Locate every uninfected red blood cell.
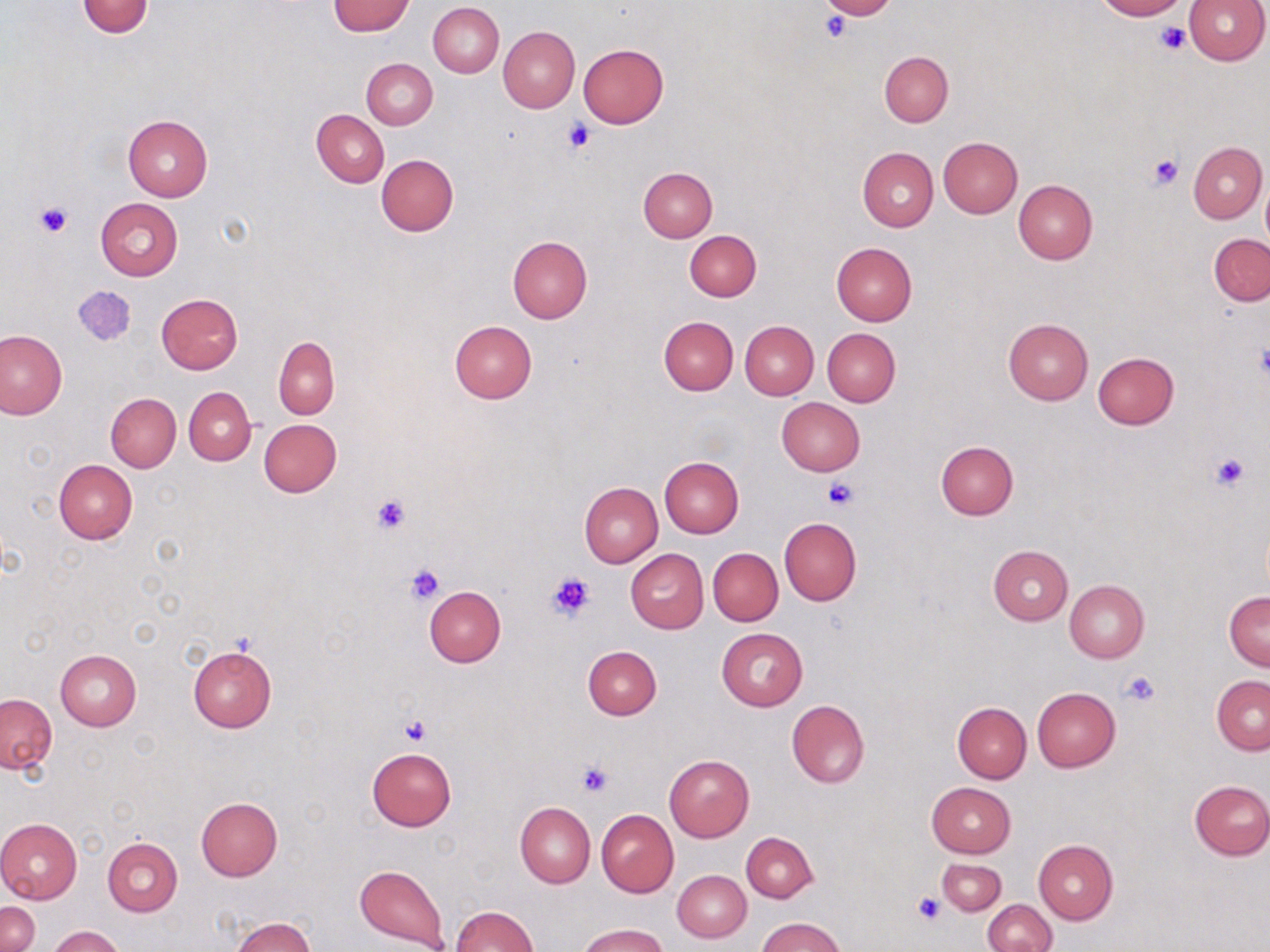
Approximate bounding boxes as named x1/y1/x2/y2 corners in pixels.
Uninfected red blood cells: (x1=819, y1=0, x2=898, y2=20), (x1=1093, y1=0, x2=1188, y2=20), (x1=1182, y1=0, x2=1269, y2=64), (x1=75, y1=1, x2=154, y2=38), (x1=327, y1=1, x2=414, y2=35), (x1=428, y1=3, x2=504, y2=78), (x1=499, y1=26, x2=579, y2=113), (x1=577, y1=44, x2=668, y2=128), (x1=879, y1=51, x2=953, y2=126), (x1=363, y1=58, x2=437, y2=128), (x1=313, y1=109, x2=389, y2=187), (x1=123, y1=115, x2=213, y2=202), (x1=938, y1=138, x2=1022, y2=218), (x1=1188, y1=142, x2=1266, y2=222), (x1=858, y1=146, x2=938, y2=232), (x1=376, y1=154, x2=458, y2=237), (x1=639, y1=167, x2=717, y2=242), (x1=1261, y1=178, x2=1270, y2=249), (x1=1013, y1=180, x2=1097, y2=265), (x1=96, y1=199, x2=183, y2=281), (x1=685, y1=230, x2=761, y2=301), (x1=1209, y1=234, x2=1270, y2=306), (x1=507, y1=236, x2=593, y2=323), (x1=831, y1=242, x2=918, y2=325), (x1=157, y1=293, x2=243, y2=375), (x1=658, y1=316, x2=738, y2=395), (x1=1004, y1=318, x2=1093, y2=404), (x1=450, y1=320, x2=537, y2=403), (x1=740, y1=321, x2=819, y2=400), (x1=822, y1=328, x2=901, y2=407), (x1=0, y1=330, x2=66, y2=419), (x1=274, y1=336, x2=339, y2=418), (x1=1091, y1=351, x2=1180, y2=430), (x1=184, y1=387, x2=255, y2=465), (x1=106, y1=394, x2=181, y2=472), (x1=776, y1=397, x2=866, y2=476), (x1=258, y1=419, x2=342, y2=497), (x1=935, y1=440, x2=1018, y2=520), (x1=659, y1=457, x2=744, y2=538), (x1=53, y1=460, x2=137, y2=544), (x1=579, y1=482, x2=663, y2=567), (x1=779, y1=518, x2=860, y2=605), (x1=988, y1=545, x2=1073, y2=625), (x1=708, y1=547, x2=782, y2=626), (x1=625, y1=549, x2=709, y2=633), (x1=1065, y1=581, x2=1149, y2=663), (x1=423, y1=586, x2=506, y2=667), (x1=1224, y1=591, x2=1270, y2=670), (x1=717, y1=629, x2=808, y2=710), (x1=188, y1=645, x2=276, y2=732), (x1=583, y1=645, x2=661, y2=720), (x1=56, y1=650, x2=141, y2=729), (x1=1212, y1=675, x2=1270, y2=755), (x1=1032, y1=687, x2=1120, y2=771), (x1=1, y1=693, x2=57, y2=774), (x1=786, y1=699, x2=870, y2=787), (x1=952, y1=701, x2=1032, y2=782), (x1=367, y1=748, x2=456, y2=830), (x1=664, y1=755, x2=754, y2=841), (x1=1189, y1=780, x2=1269, y2=860), (x1=927, y1=782, x2=1016, y2=858), (x1=196, y1=797, x2=283, y2=880), (x1=515, y1=803, x2=595, y2=888), (x1=596, y1=810, x2=679, y2=896), (x1=0, y1=817, x2=82, y2=905), (x1=742, y1=832, x2=817, y2=903), (x1=102, y1=838, x2=182, y2=916), (x1=1033, y1=840, x2=1117, y2=925), (x1=936, y1=858, x2=1007, y2=915), (x1=354, y1=863, x2=448, y2=952), (x1=673, y1=870, x2=750, y2=943), (x1=983, y1=899, x2=1057, y2=952), (x1=1, y1=901, x2=39, y2=952), (x1=450, y1=905, x2=538, y2=952), (x1=757, y1=916, x2=846, y2=952), (x1=231, y1=917, x2=315, y2=952), (x1=579, y1=924, x2=668, y2=952), (x1=49, y1=926, x2=124, y2=952).

Summary:
  - Platelet locations: (x1=821, y1=12, x2=851, y2=41), (x1=1155, y1=22, x2=1190, y2=55), (x1=562, y1=119, x2=596, y2=154), (x1=1146, y1=153, x2=1182, y2=191), (x1=36, y1=201, x2=71, y2=238), (x1=1257, y1=342, x2=1270, y2=385), (x1=1209, y1=451, x2=1251, y2=491), (x1=822, y1=478, x2=858, y2=509), (x1=370, y1=493, x2=412, y2=538), (x1=405, y1=563, x2=445, y2=605), (x1=547, y1=571, x2=593, y2=621), (x1=1119, y1=669, x2=1161, y2=706), (x1=401, y1=716, x2=431, y2=746), (x1=576, y1=763, x2=613, y2=797), (x1=914, y1=893, x2=946, y2=923)
  - Slide-level diagnosis: no evidence of blood parasites
  - Image size: 1270×952 pixels
  - Magnification: 1000x
  - Modality: light microscopy
  - Field of view: one of a larger specimen
  - Preparation: thin blood film
  - Stain: May-Grünwald-Giemsa